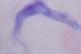

{
  "modality": "micrograph",
  "magnification": "1000x",
  "identification": "trypanosome"
}